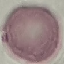

Summary:
  - Result: no malaria parasites detected
  - Stain: Giemsa
  - Preparation: thin blood film
  - Capture: smartphone through the microscope eyepiece
  - Image type: cell patch, automatically extracted from a larger field of view and resized to 64 × 64 pixels